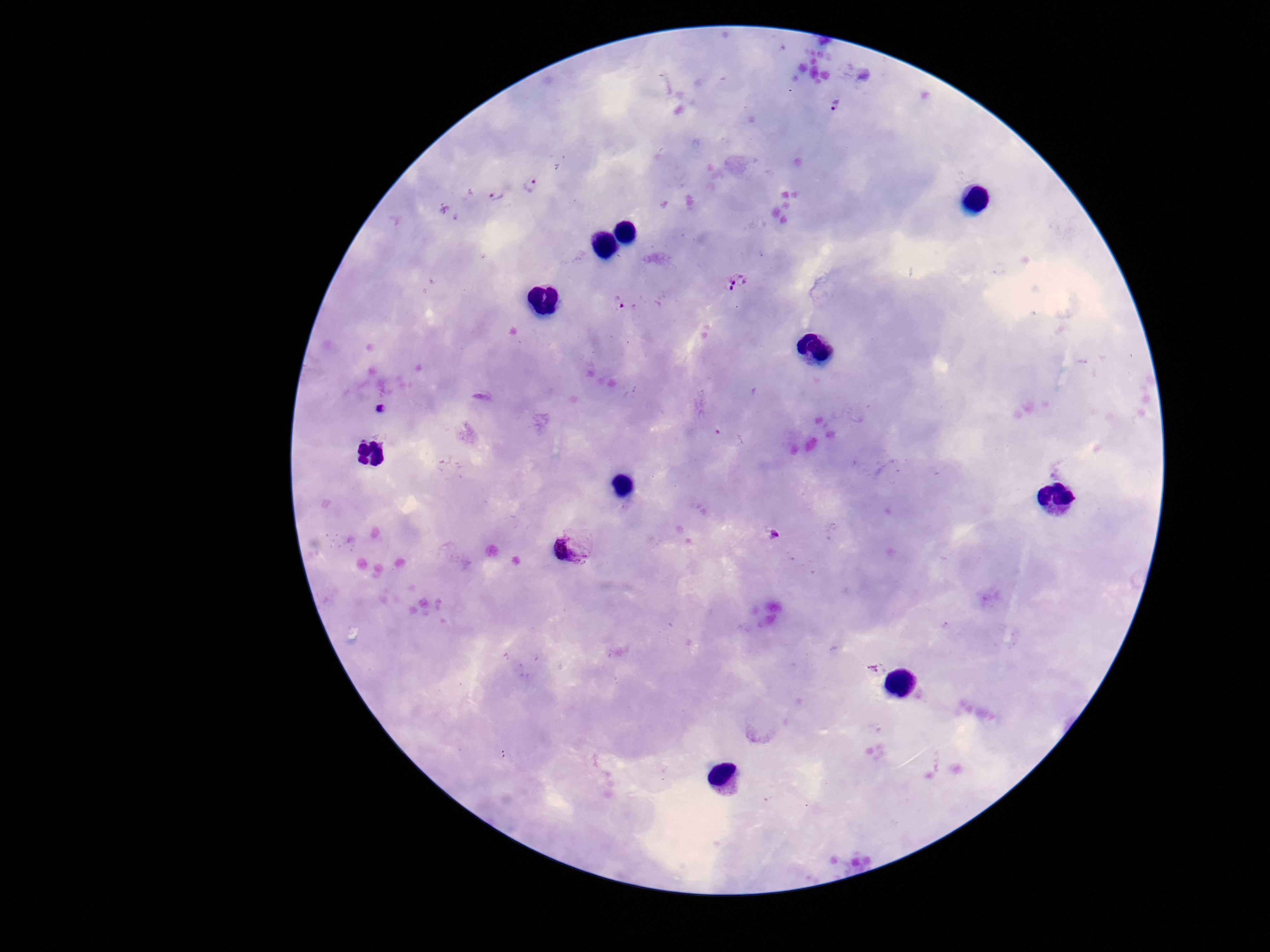
{
  "preparation": "thick peripheral-blood smear",
  "magnification": "100x",
  "stain": "Giemsa",
  "capture": "smartphone camera through the microscope eyepiece",
  "field_of_view": "one from this slide",
  "plasmodium_parasite_locations": "approximate centers as (x, y) in pixels: (833, 105), (531, 185), (494, 194), (739, 278), (727, 290), (618, 301), (568, 550)",
  "image_size": "1270×952 pixels",
  "patient_malaria_status": "infected"
}